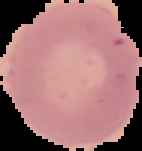
Summary:
  - Result: no malaria parasites detected
  - Image size: 142×151 pixels
  - Image type: segmented cell region with the area outside set to black
  - Preparation: thin blood film